Assess the morphology of the erythrocytes.
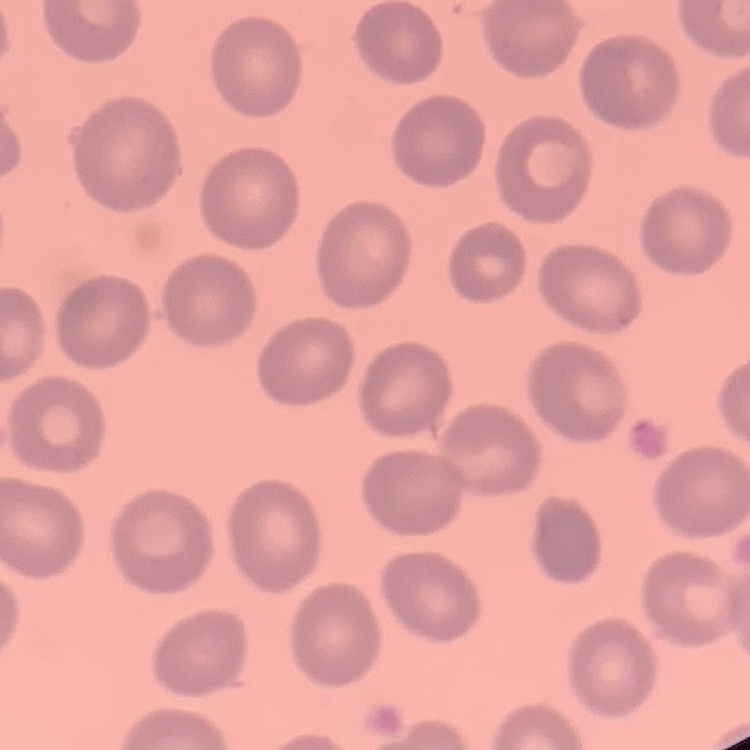

They show no rouleaux formation.

Thin blood smear. Stained with either Field's or Giemsa. One tile cut from a larger photomicrograph.